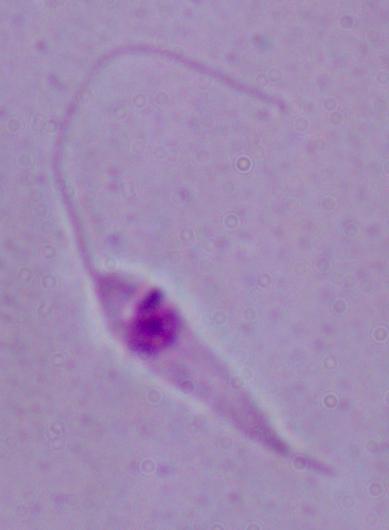
Micrograph. 1000x magnification. A Leishmania parasite is seen.